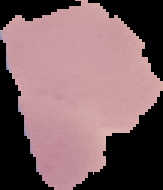
{
  "preparation": "thin blood film",
  "image_type": "segmented cell region with the area outside set to black",
  "malaria_status": "uninfected",
  "image_size": "163×190 pixels"
}